Assess this cell for malaria.
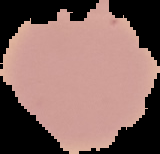
It is uninfected.

image type = cell region segmented out of the field of view; surrounding area masked to black
image size = 160×154 pixels
preparation = thin blood smear